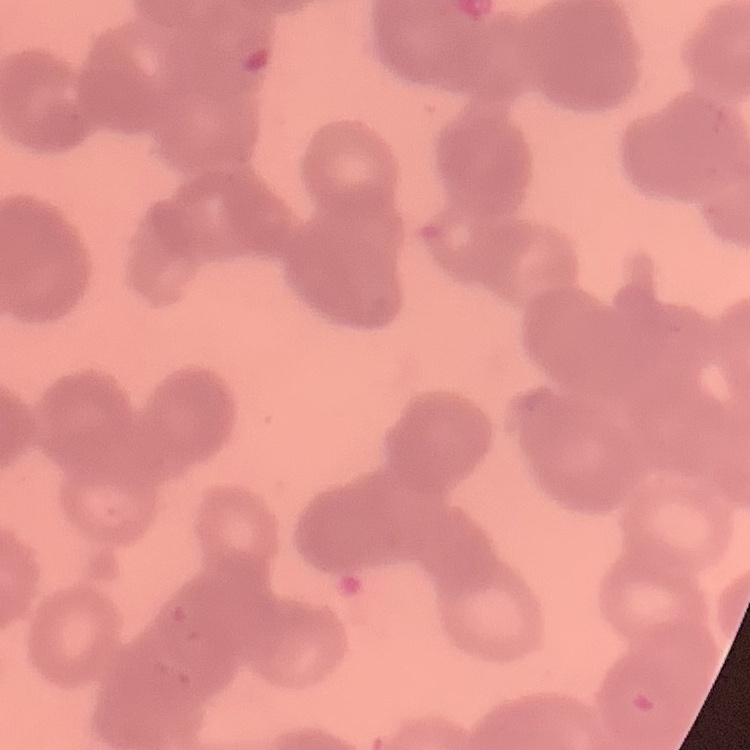

The red blood cells exhibit rouleaux formation. One tile cut from a larger photomicrograph. Thin peripheral smear. Field's or Giemsa stain.